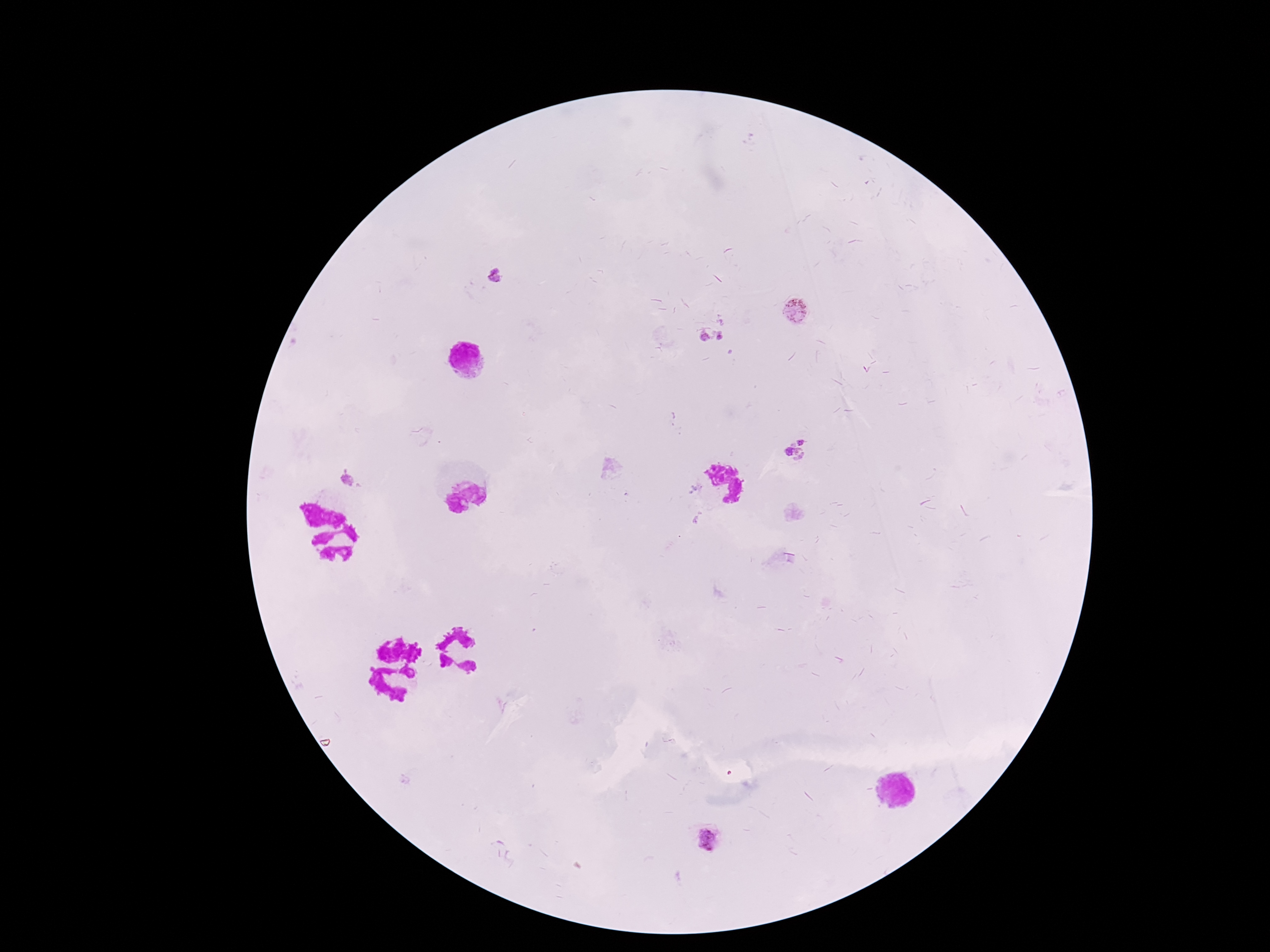
Approximate centers as [x, y] in pixels.
Summary:
  - Plasmodium parasite locations: [494, 275], [795, 310], [721, 336], [705, 337], [796, 450], [348, 479]
  - Preparation: thick peripheral-blood smear
  - Image size: 1270×952 pixels
  - Capture: smartphone camera through the microscope eyepiece
  - Magnification: 100x
  - Stain: Giemsa
  - Field of view: one from this slide
  - Patient malaria status: positive